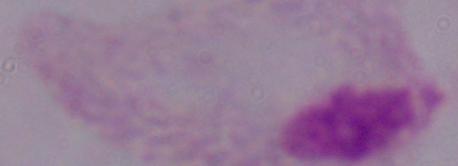

{
  "identification": "trichomonad",
  "magnification": "1000x",
  "modality": "photomicrograph"
}